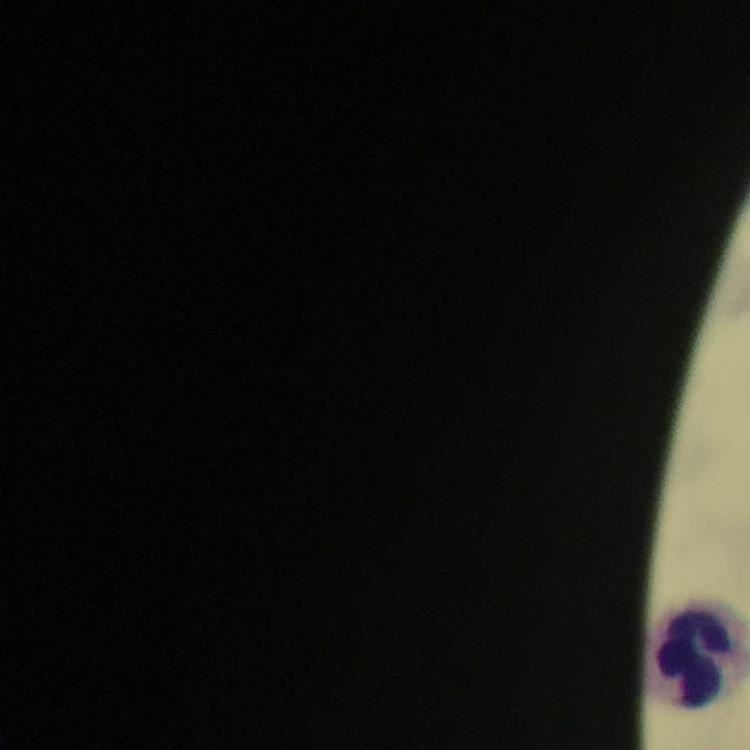
Plasmodium parasites = none detected
preparation = thick smear
immersion oil = applied
stain = Giemsa
cropped from = a single field of view
magnification = 100x
capture = smartphone camera through the microscope
image size = 750×750 pixels
context = from a diagnostic examination for malaria
leukocyte locations = approximate centers as [x, y] in pixels: [699, 657]